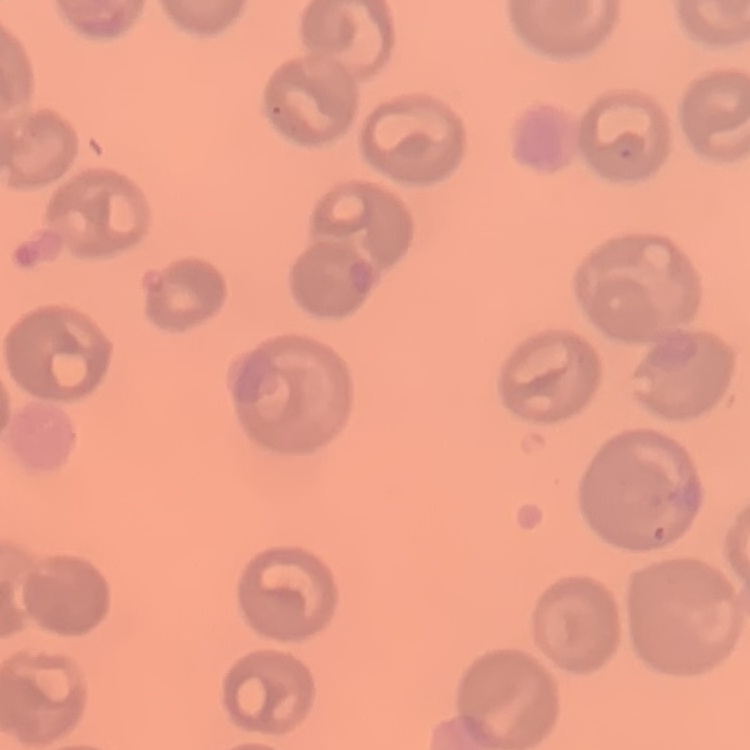
erythrocyte morphology = no rouleaux formation
stain = Field's or Giemsa
preparation = thin peripheral smear
image type = square crop of a larger photomicrograph